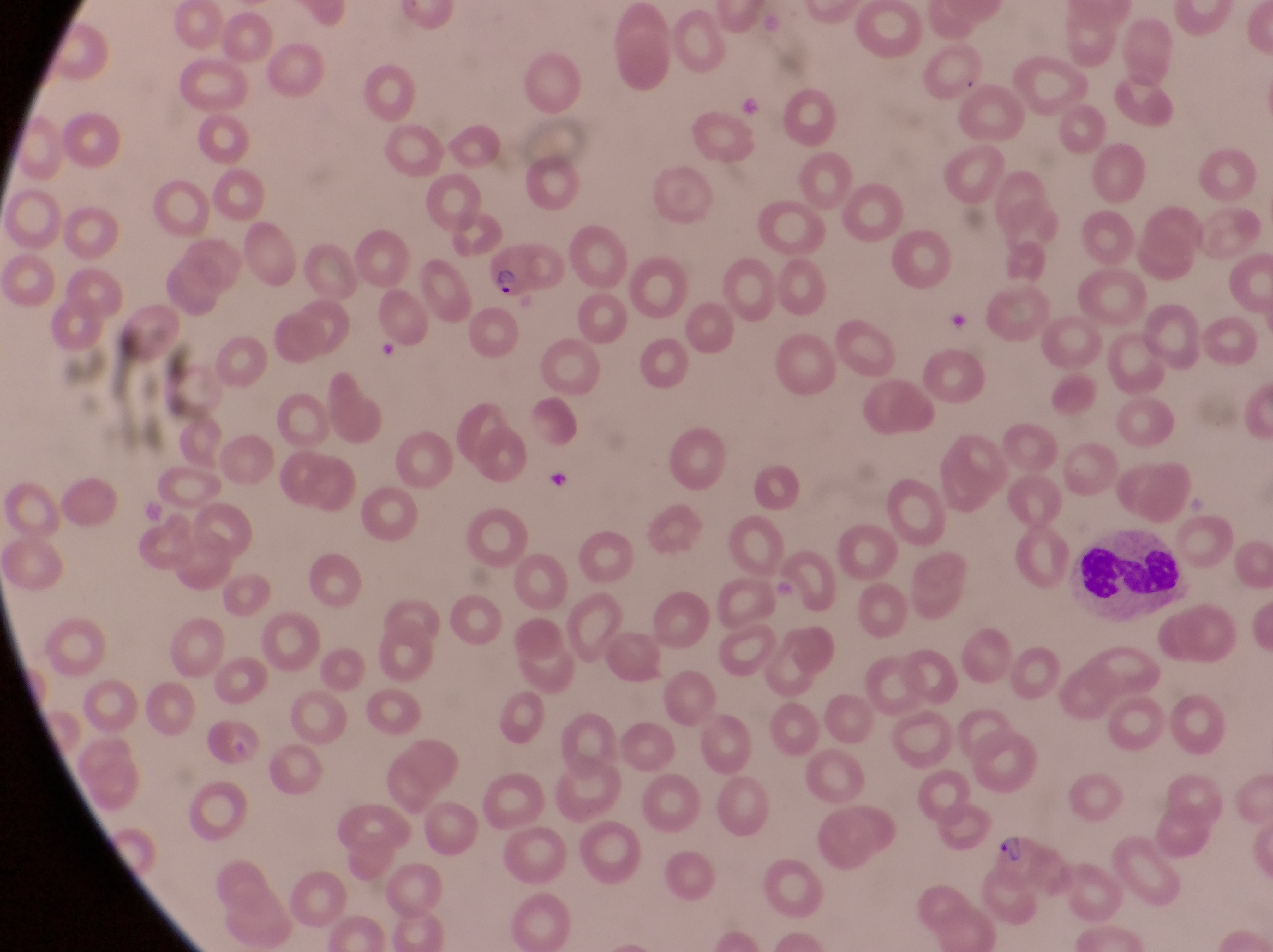
Approximate bounding boxes as (left, top, right, bottom) in pixels.
Summary:
  - Artifact (platelet-like body, stain precipitate, or debris) locations: (941, 302, 969, 337)
  - Parasitised red blood cell locations: (487, 242, 567, 307), (991, 834, 1053, 886)
  - Trophozoite locations: (544, 469, 577, 497)
  - Leukocyte locations: (1078, 527, 1185, 617)
  - Capture: smartphone photograph through the eyepiece of an Olympus CX-23 microscope
  - Magnification: 1000x
  - Country: Uganda
  - Image size: 1273×952 pixels
  - Field of view: single
  - Preparation: thin blood smear